Report the malaria status of this cell.
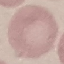
It is uninfected.

Photographed with a smartphone camera at the microscope eyepiece. Automatically extracted cell patch, resized to 64 × 64 pixels. Giemsa-stained preparation. Thin blood smear.